Assess this cell for malaria.
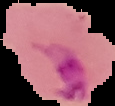
It is parasitized.

Summary:
  - Image type: segmented cell region on a black background
  - Preparation: thin blood film
  - Image size: 115×106 pixels